Locate every malaria parasite and every leukocyte.
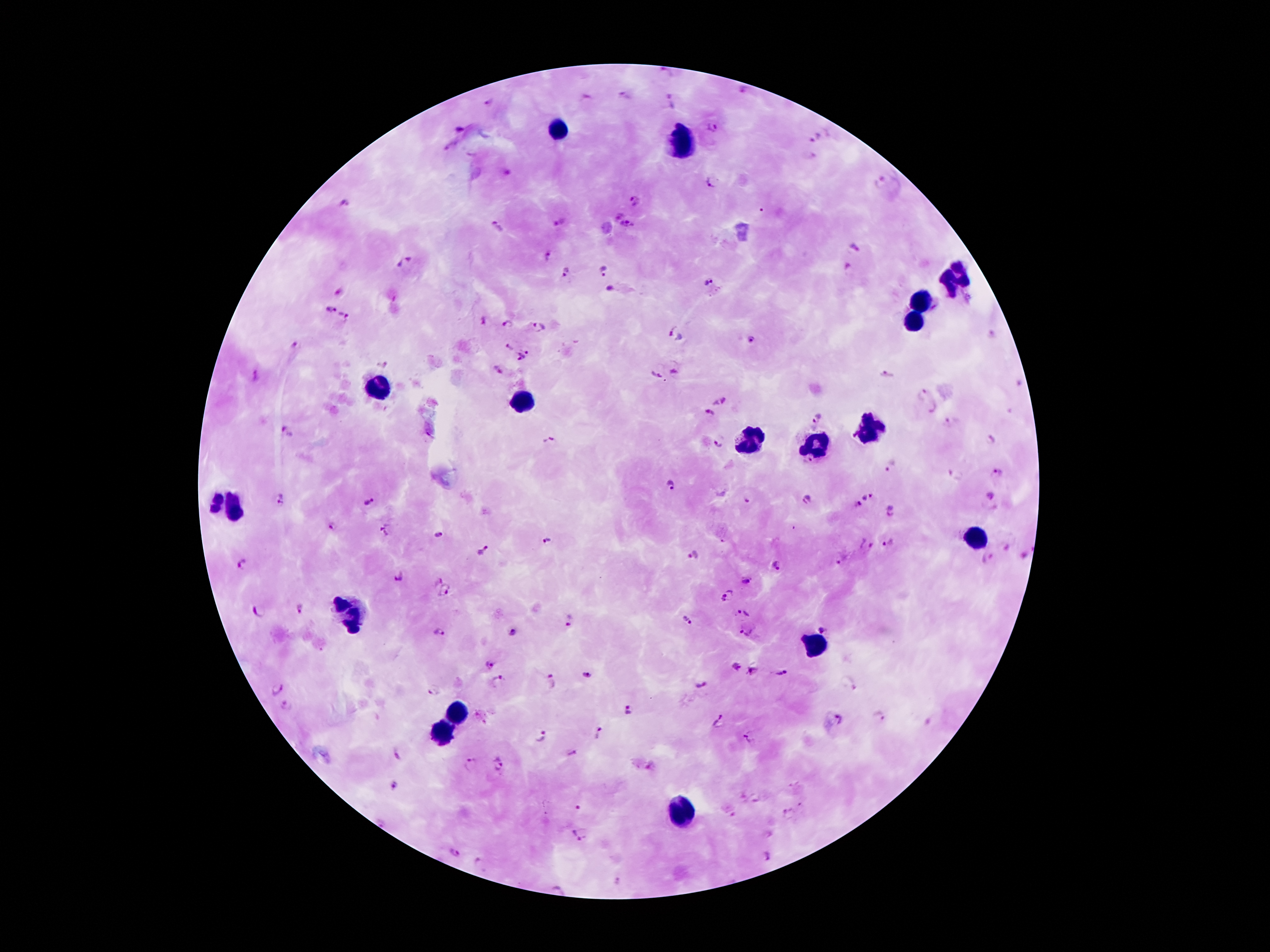

Approximate centers as {x, y} in pixels.
Malaria parasites: {666, 71}, {743, 90}, {624, 95}, {670, 103}, {488, 104}, {712, 127}, {817, 139}, {880, 183}, {709, 185}, {636, 201}, {343, 205}, {617, 216}, {560, 224}, {627, 226}, {497, 228}, {855, 248}, {548, 257}, {404, 262}, {847, 270}, {603, 271}, {567, 272}, {708, 281}, {609, 288}, {330, 311}, {344, 317}, {483, 320}, {508, 325}, {540, 327}, {670, 330}, {990, 336}, {750, 341}, {295, 346}, {509, 349}, {528, 352}, {520, 356}, {383, 364}, {498, 369}, {674, 373}, {657, 376}, {887, 376}, {256, 377}, {921, 395}, {718, 402}, {931, 408}, {708, 413}, {818, 417}, {948, 423}, {289, 432}, {991, 439}, {550, 440}, {718, 444}, {891, 465}, {996, 474}, {956, 477}, {672, 485}, {991, 494}, {866, 496}, {280, 499}, {806, 499}, {370, 502}, {748, 502}, {857, 505}, {891, 511}, {332, 525}, {387, 530}, {438, 536}, {547, 542}, {890, 543}, {865, 546}, {484, 552}, {693, 555}, {987, 558}, {837, 560}, {243, 564}, {778, 566}, {399, 577}, {437, 580}, {744, 581}, {446, 592}, {726, 596}, {299, 607}, {259, 611}, {743, 611}, {687, 620}, {569, 621}, {823, 627}, {747, 632}, {440, 633}, {511, 633}, {490, 663}, {751, 671}, {586, 674}, {782, 674}, {498, 680}, {551, 682}, {703, 685}, {277, 689}, {433, 689}, {286, 705}, {629, 709}, {880, 718}, {841, 719}, {720, 721}, {598, 733}, {541, 737}, {750, 738}, {572, 753}, {397, 756}, {470, 763}, {499, 764}, {394, 786}, {578, 808}, {789, 814}, {577, 833}, {454, 853}, {768, 857}, {477, 862}, {617, 880}.
Leukocytes: {558, 129}, {680, 147}, {954, 278}, {920, 301}, {913, 321}, {383, 386}, {519, 406}, {870, 425}, {752, 440}, {815, 444}, {225, 503}, {982, 535}, {350, 614}, {817, 646}, {456, 714}, {444, 733}, {679, 814}.

magnification = 100x
capture = smartphone through the microscope eyepiece
preparation = thick blood film
image size = 1270×952 pixels
patient malaria status = infected with Plasmodium falciparum
field of view = one from this slide
stain = Giemsa